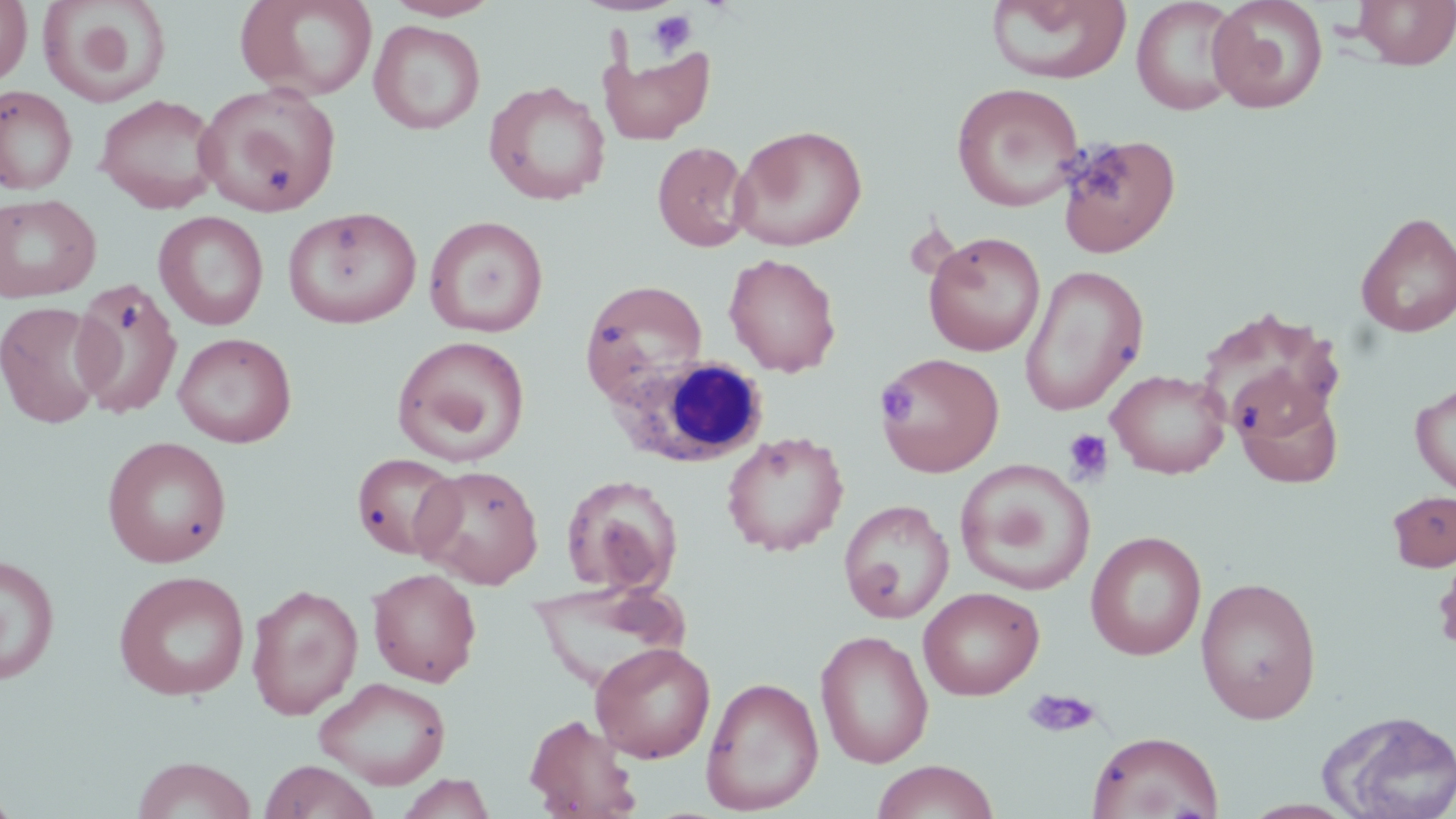 Approximate bounding boxes as [x1, y1, x2, y2] in pixels. White blood cell locations: [607, 355, 770, 469]. Uninfected red blood cell locations: [0, 0, 32, 88], [36, 0, 171, 108], [236, 0, 378, 101], [383, 0, 501, 21], [984, 0, 1133, 85], [1132, 0, 1243, 116], [1207, 0, 1329, 114], [1351, 0, 1456, 71], [369, 20, 485, 135], [598, 42, 715, 144], [483, 80, 611, 206], [194, 82, 341, 216], [951, 82, 1086, 212], [0, 85, 77, 195], [94, 94, 223, 213], [732, 124, 868, 251], [1057, 134, 1181, 257], [652, 141, 753, 252], [0, 193, 101, 303], [282, 206, 421, 329], [154, 211, 269, 330], [1355, 211, 1456, 338], [424, 215, 549, 337], [923, 231, 1046, 357], [724, 253, 842, 377], [1019, 264, 1149, 416], [70, 278, 183, 419], [579, 278, 709, 406], [1, 301, 109, 429], [1194, 306, 1346, 442], [172, 332, 297, 448], [391, 335, 531, 467], [876, 351, 1004, 477], [1106, 368, 1231, 478], [1410, 380, 1456, 497], [1236, 385, 1344, 490], [721, 431, 849, 556], [101, 436, 232, 568], [351, 452, 462, 560], [955, 459, 1096, 596], [412, 463, 545, 589], [561, 474, 684, 597], [1387, 490, 1456, 572], [838, 499, 954, 623], [1085, 530, 1207, 660], [1435, 545, 1456, 657], [0, 553, 60, 686], [367, 568, 482, 687], [113, 570, 251, 701], [1195, 576, 1322, 723], [526, 580, 693, 687], [247, 584, 363, 720], [919, 586, 1044, 700], [815, 629, 934, 768], [591, 642, 715, 763], [313, 676, 451, 789], [701, 676, 824, 814], [1317, 709, 1456, 819], [524, 713, 642, 819], [1087, 730, 1223, 818], [132, 756, 256, 819], [258, 760, 380, 819], [871, 760, 1000, 819], [395, 773, 497, 818], [0, 785, 22, 819]. Platelet locations: [646, 10, 697, 57], [876, 382, 917, 424], [1063, 428, 1114, 484], [1021, 689, 1102, 738]. Slide-level diagnosis: negative for blood parasites. Image is 1456×819 pixels. Optical microscopy. One field of a larger specimen. 1000x magnification. May-Grünwald-Giemsa-stained preparation. Thin blood film.